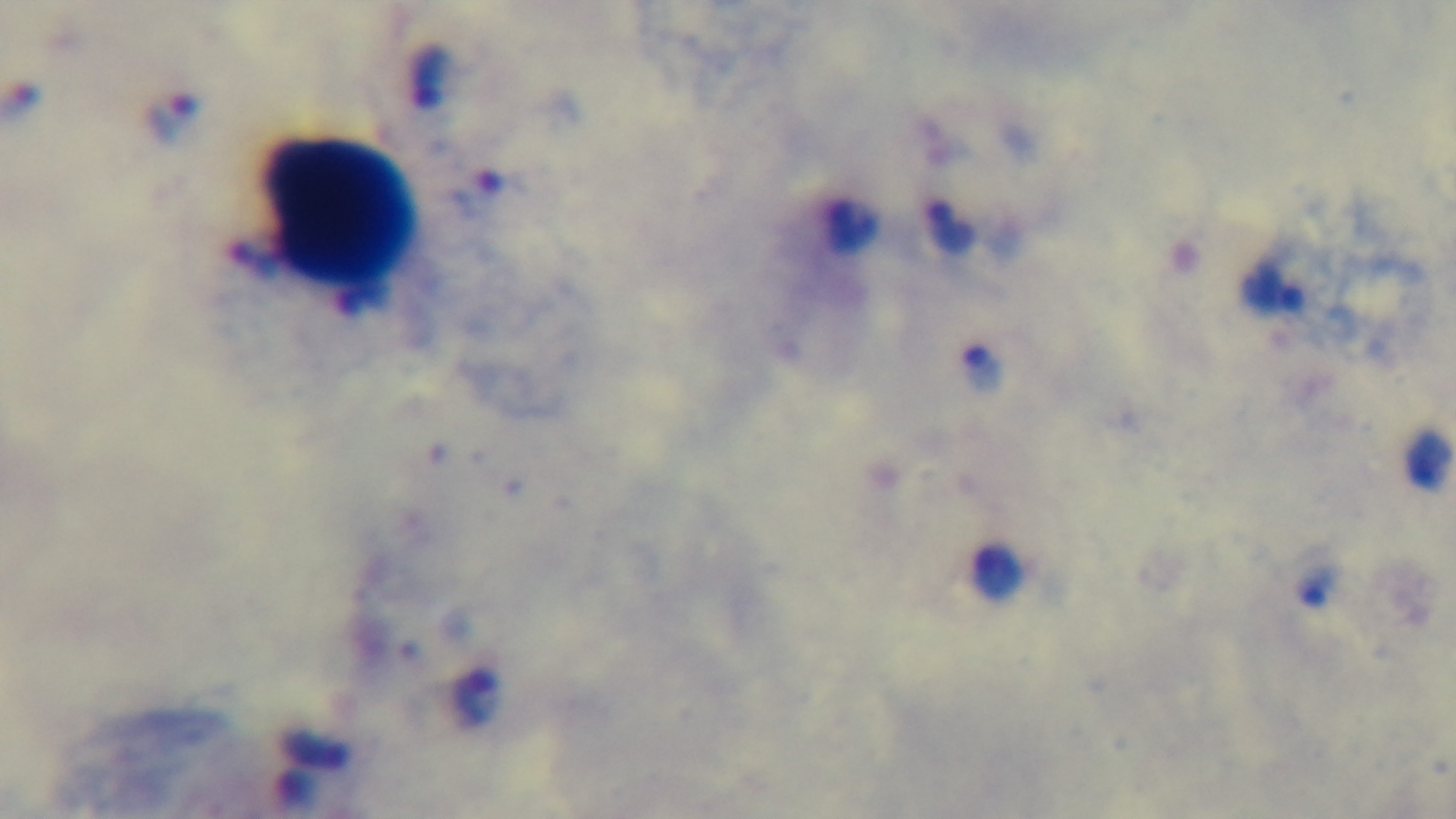 100x oil-immersion objective. Giemsa stain. Preparation: thick smear. Malaria status: infected. Light microscopy. Single field of view. Mounted 4K digital camera.